Report the malaria status of this cell.
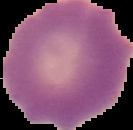
It is uninfected.

Summary:
  - Preparation: thin blood film
  - Image type: segmented cell region on a black background
  - Image size: 133×130 pixels